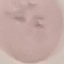 Result: no malaria parasites detected. Giemsa stain. Photographed with a smartphone camera at the microscope eyepiece. Thin blood film. Cell patch, automatically extracted from a larger field of view and resized to 64 × 64 pixels.